Report the malaria status of this cell.
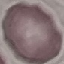

Uninfected.

Giemsa stain. Acquired by smartphone through the microscope eyepiece. Automatically extracted cell patch, resized to 64 × 64 pixels. Thin blood smear.